Give the position of every malaria parasite.
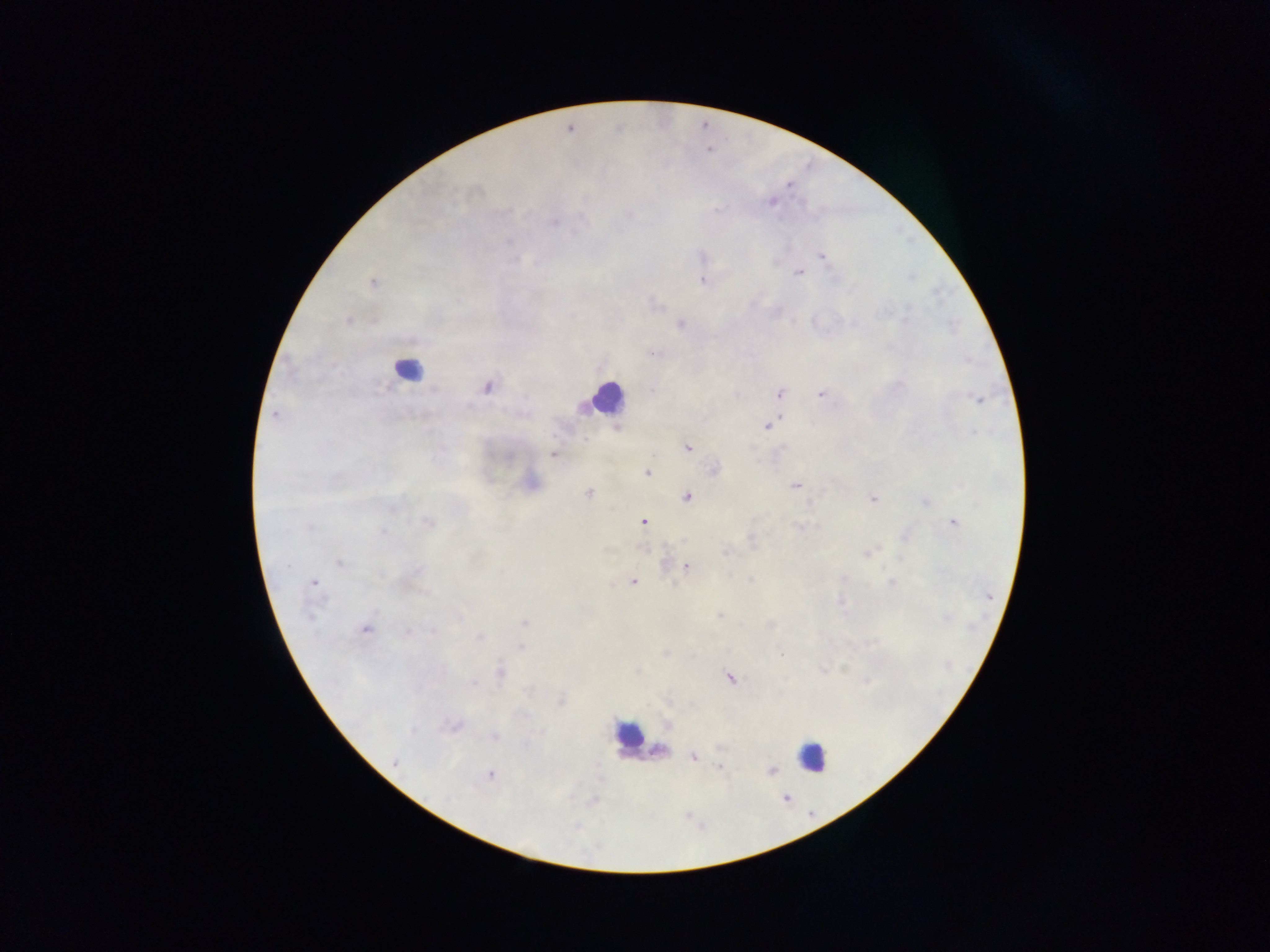
Approximate centers as (x, y) in pixels.
Malaria parasites: (788, 186), (474, 195), (770, 201), (717, 210), (508, 212), (629, 214), (555, 220), (510, 241), (820, 257), (515, 260), (775, 262), (798, 273), (911, 277), (702, 281), (371, 282), (655, 303), (910, 305), (350, 322), (680, 323), (953, 326), (487, 387), (781, 392), (819, 393), (979, 401), (273, 416), (779, 418), (765, 425), (688, 449), (552, 455), (647, 473), (795, 486), (588, 493), (688, 498), (871, 500), (392, 510), (955, 521), (643, 522), (428, 523), (308, 527), (800, 527), (383, 533), (751, 541), (726, 553), (866, 553), (339, 563), (288, 566), (687, 567), (729, 573), (750, 580), (633, 581), (674, 582), (893, 582), (313, 583), (840, 600), (718, 615), (311, 618), (524, 623), (772, 626), (365, 630), (431, 631), (406, 632), (479, 638), (522, 647), (666, 653), (782, 654), (845, 668), (637, 670), (824, 670), (500, 672), (729, 678), (868, 681), (472, 685), (561, 701), (451, 727), (545, 732), (496, 737), (658, 751), (694, 758), (393, 764), (721, 768), (772, 770), (489, 774), (575, 827).

Leukocyte locations: (407, 373), (604, 401), (624, 737), (812, 761). Image is 1270×952 pixels. Thick blood smear. Photographed through a microscope with a mobile-phone camera. One field of view. Collected in Ghana.